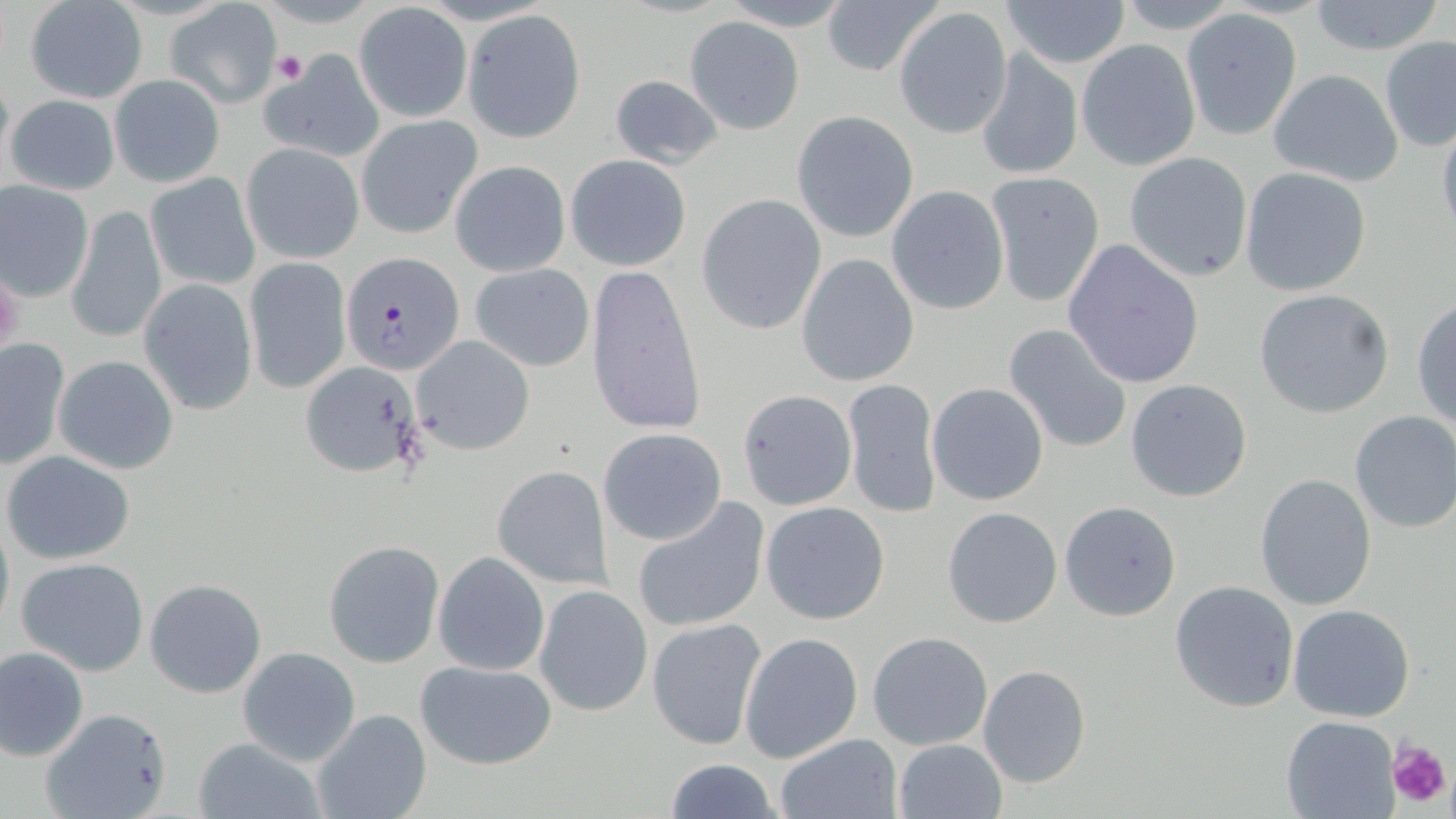

Plasmodium falciparum-infected red blood cell locations = approximate bounding boxes as (x1,y1)-(x2,y2) corner pairs in pixels: (341,251)-(465,376)
slide-level diagnosis = Plasmodium falciparum
image size = 1456×819 pixels
stain = May-Grünwald-Giemsa
modality = optical microscopy
preparation = thin blood film
uninfected red blood cell locations = approximate bounding boxes as (x1,y1)-(x2,y2) corner pairs in pixels: (1000,0)-(1132,70), (1305,0)-(1447,55), (23,2)-(148,103), (821,2)-(943,78), (166,3)-(282,106), (354,4)-(471,123), (893,6)-(1014,140), (1180,9)-(1303,140), (462,10)-(586,141), (685,16)-(804,133), (1379,36)-(1456,150), (1077,39)-(1201,171), (975,49)-(1084,181), (260,51)-(383,163), (1267,68)-(1404,187), (607,72)-(726,169), (108,74)-(225,187), (4,92)-(120,195), (792,110)-(919,242), (1436,114)-(1456,242), (357,115)-(483,239), (240,141)-(365,264), (1124,151)-(1254,282), (565,154)-(691,271), (449,161)-(572,276), (1240,167)-(1372,298), (145,171)-(260,291), (984,171)-(1106,307), (0,179)-(94,300), (886,185)-(1010,315), (697,193)-(828,334), (66,203)-(167,345), (1062,237)-(1206,389), (797,253)-(921,388), (245,257)-(350,394), (584,262)-(705,436), (469,263)-(595,372), (138,279)-(258,414), (1252,289)-(1394,418), (1413,298)-(1456,432), (1003,323)-(1134,454), (411,335)-(535,457), (0,336)-(70,468), (51,353)-(182,475), (304,366)-(421,475), (842,376)-(941,520), (1124,378)-(1253,503), (926,382)-(1049,506), (737,389)-(857,511), (1349,410)-(1456,533), (597,427)-(727,546), (2,449)-(137,565), (490,463)-(615,590), (1254,473)-(1377,610), (630,496)-(770,635), (760,500)-(891,625), (1058,501)-(1182,622), (941,506)-(1064,628), (0,509)-(13,637), (324,540)-(444,667), (433,552)-(550,676), (15,556)-(151,676), (144,578)-(268,699), (1169,580)-(1299,712), (534,584)-(653,715), (1287,603)-(1416,722), (648,618)-(767,750), (738,630)-(864,763), (868,631)-(995,750), (0,645)-(89,760), (238,647)-(360,765), (414,660)-(558,771), (977,665)-(1091,788), (312,707)-(432,819), (41,708)-(171,819), (1280,715)-(1400,818), (775,733)-(903,818), (192,737)-(324,819), (894,739)-(1008,819), (664,758)-(781,818)
magnification = 1000x
platelet locations = approximate bounding boxes as (x1,y1)-(x2,y2) corner pairs in pixels: (272,50)-(309,86), (1386,741)-(1450,811)
field of view = one of a larger specimen